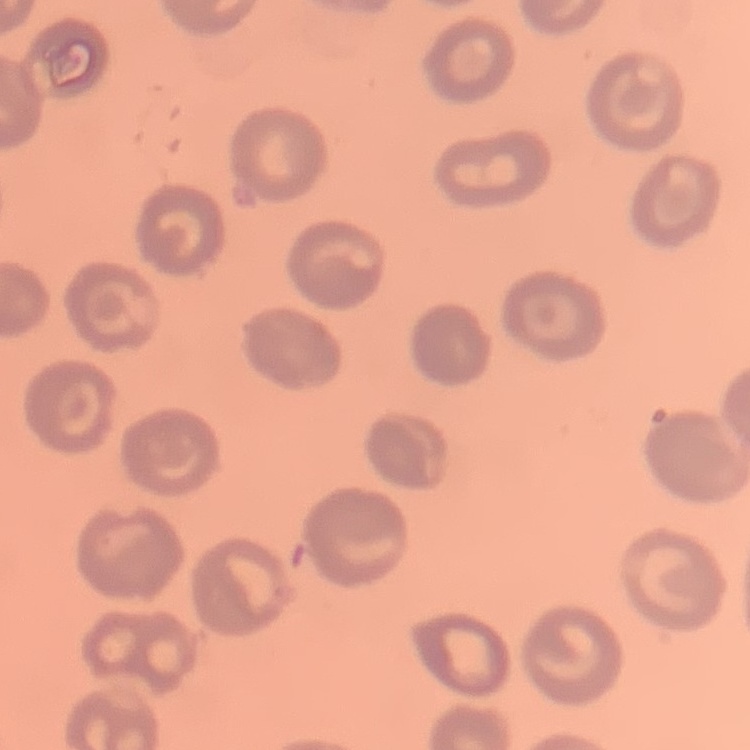

Summary:
  - Red blood cell morphology: no rouleaux formation
  - Stain: Field's or Giemsa
  - Preparation: thin peripheral smear
  - Image type: one tile cut from a larger photomicrograph